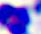

Summary:
  - Magnification: 400x
  - Identification: white blood cell
  - Modality: photomicrograph